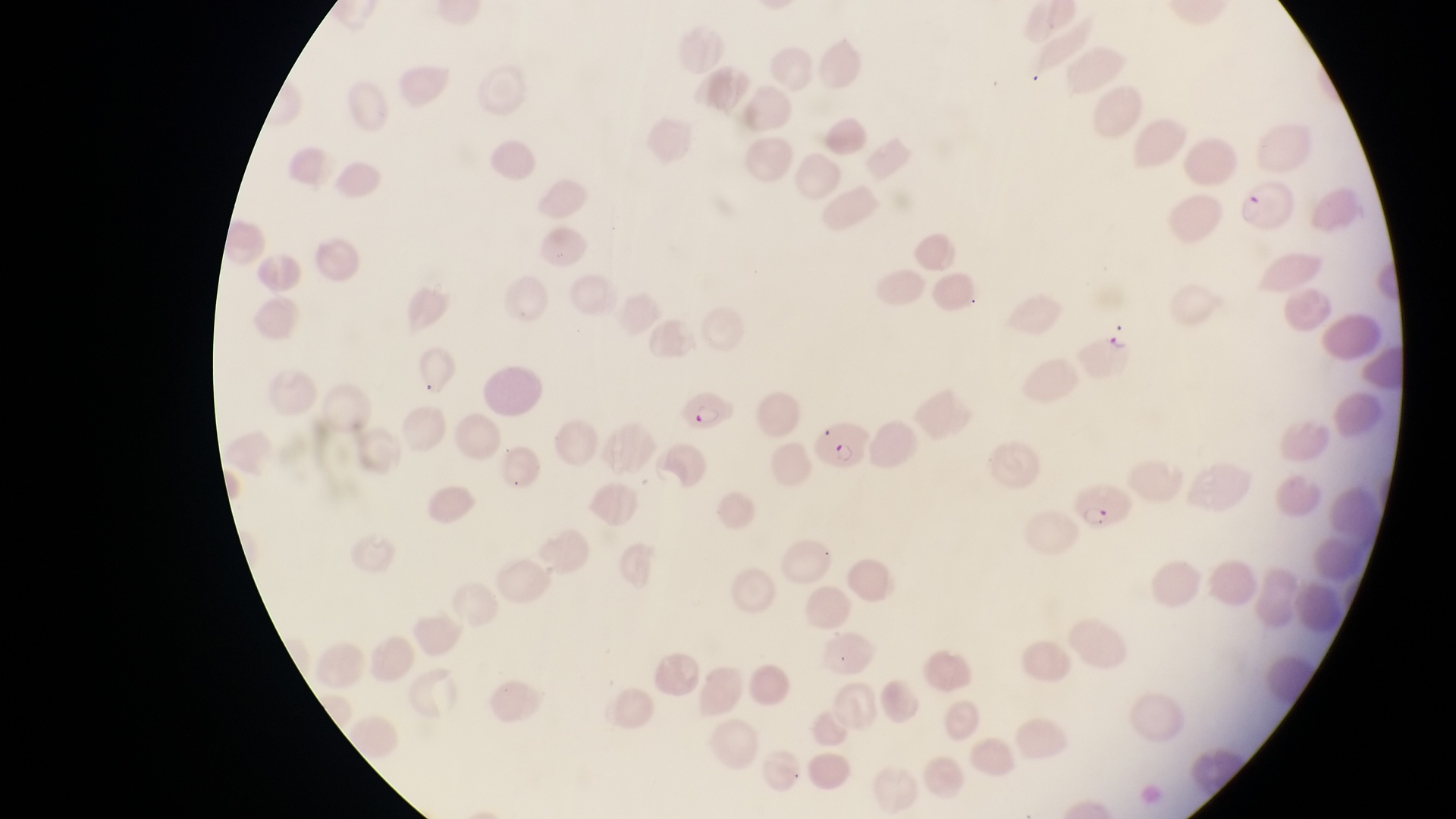

Approximate bounding boxes as {left, top, right, bottom} in pixels. Parasitised red blood cell locations: {1234, 179, 1294, 235}, {1076, 331, 1147, 383}, {680, 383, 738, 433}, {816, 425, 872, 478}, {1076, 482, 1132, 531}. One field of view. Captured by a smartphone held over the eyepiece of an Olympus CX-23 microscope. Magnification of 1000x. Image is 1456×819 pixels. Collected in Uganda. Thin blood film.